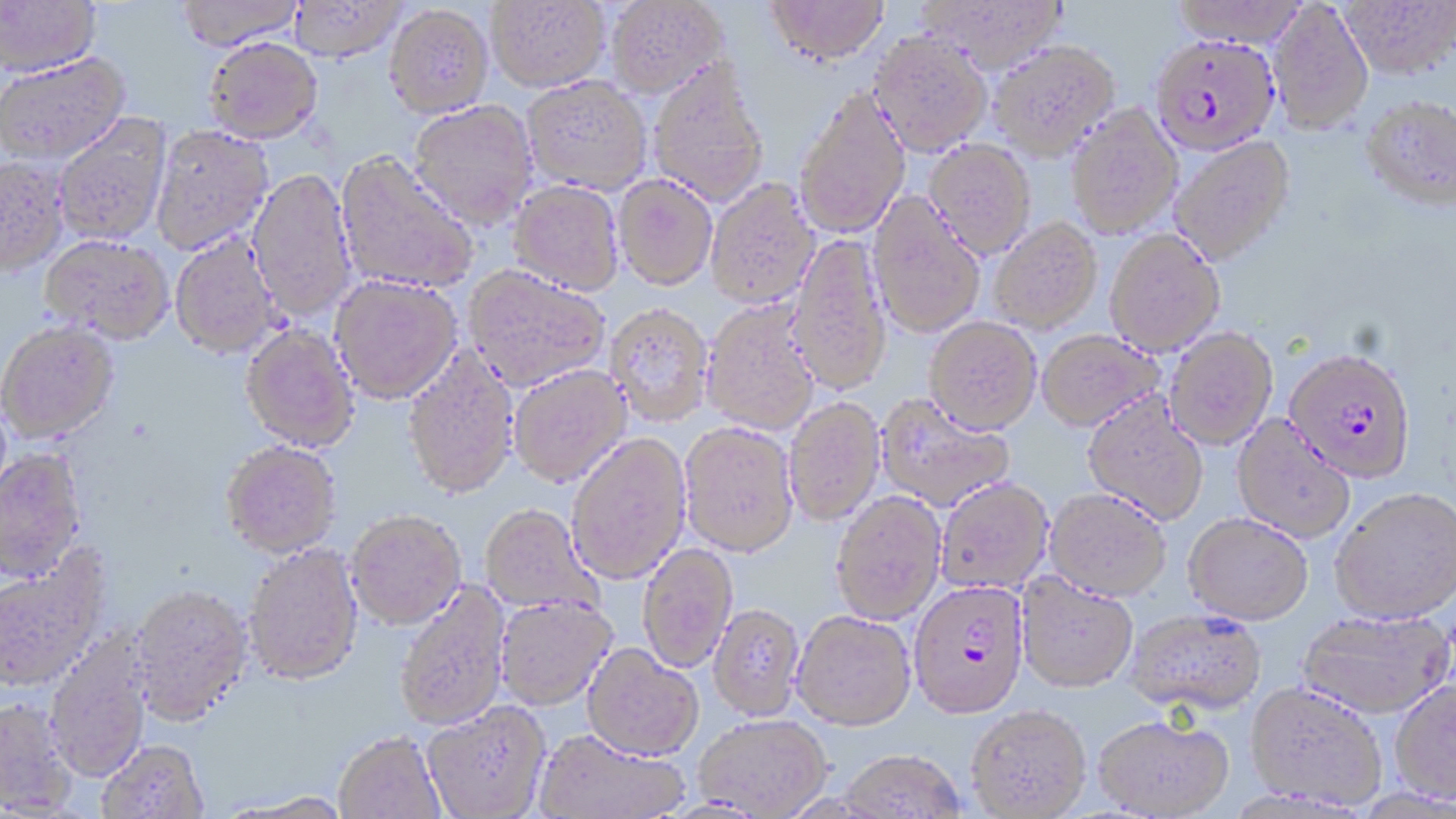 Approximate bounding boxes as named x1/y1/x2/y2 corners in pixels. Uninfected red blood cell locations: (x1=0, y1=0, x2=101, y2=77), (x1=176, y1=0, x2=304, y2=50), (x1=486, y1=0, x2=610, y2=92), (x1=606, y1=0, x2=728, y2=98), (x1=764, y1=0, x2=889, y2=66), (x1=918, y1=0, x2=1070, y2=73), (x1=1170, y1=0, x2=1308, y2=48), (x1=1339, y1=0, x2=1455, y2=78), (x1=288, y1=1, x2=407, y2=61), (x1=1268, y1=2, x2=1373, y2=134), (x1=384, y1=4, x2=494, y2=117), (x1=869, y1=31, x2=992, y2=156), (x1=204, y1=37, x2=323, y2=143), (x1=989, y1=39, x2=1120, y2=160), (x1=0, y1=52, x2=131, y2=164), (x1=648, y1=58, x2=770, y2=208), (x1=521, y1=75, x2=653, y2=194), (x1=794, y1=86, x2=911, y2=239), (x1=1360, y1=94, x2=1456, y2=211), (x1=408, y1=100, x2=539, y2=229), (x1=1066, y1=104, x2=1182, y2=238), (x1=53, y1=113, x2=172, y2=246), (x1=150, y1=124, x2=274, y2=256), (x1=1169, y1=136, x2=1296, y2=266), (x1=923, y1=139, x2=1037, y2=258), (x1=335, y1=151, x2=479, y2=294), (x1=0, y1=156, x2=69, y2=277), (x1=247, y1=167, x2=357, y2=322), (x1=613, y1=174, x2=718, y2=291), (x1=706, y1=178, x2=820, y2=308), (x1=508, y1=180, x2=624, y2=295), (x1=868, y1=192, x2=986, y2=338), (x1=990, y1=217, x2=1102, y2=333), (x1=1105, y1=229, x2=1224, y2=356), (x1=170, y1=233, x2=281, y2=358), (x1=41, y1=234, x2=174, y2=345), (x1=788, y1=234, x2=892, y2=396), (x1=464, y1=266, x2=610, y2=391), (x1=330, y1=275, x2=462, y2=403), (x1=702, y1=300, x2=820, y2=435), (x1=605, y1=304, x2=713, y2=425), (x1=924, y1=317, x2=1042, y2=434), (x1=0, y1=322, x2=120, y2=444), (x1=240, y1=324, x2=360, y2=452), (x1=1165, y1=327, x2=1279, y2=449), (x1=1036, y1=329, x2=1163, y2=431), (x1=402, y1=346, x2=520, y2=500), (x1=509, y1=365, x2=631, y2=487), (x1=876, y1=394, x2=1015, y2=512), (x1=1082, y1=394, x2=1208, y2=526), (x1=784, y1=397, x2=885, y2=526), (x1=1232, y1=416, x2=1355, y2=543), (x1=678, y1=422, x2=799, y2=556), (x1=566, y1=433, x2=691, y2=585), (x1=220, y1=440, x2=342, y2=558), (x1=0, y1=448, x2=87, y2=585), (x1=936, y1=478, x2=1054, y2=594), (x1=1044, y1=489, x2=1171, y2=601), (x1=1331, y1=489, x2=1456, y2=625), (x1=831, y1=491, x2=946, y2=624), (x1=479, y1=505, x2=603, y2=615), (x1=346, y1=509, x2=467, y2=630), (x1=1183, y1=513, x2=1313, y2=625), (x1=638, y1=542, x2=738, y2=673), (x1=243, y1=544, x2=364, y2=687), (x1=0, y1=549, x2=112, y2=695), (x1=1017, y1=573, x2=1139, y2=693), (x1=395, y1=581, x2=511, y2=732), (x1=129, y1=585, x2=253, y2=728), (x1=494, y1=596, x2=617, y2=711), (x1=708, y1=604, x2=805, y2=720), (x1=1124, y1=609, x2=1267, y2=717), (x1=1296, y1=609, x2=1453, y2=720), (x1=792, y1=611, x2=916, y2=733), (x1=45, y1=637, x2=152, y2=784), (x1=583, y1=644, x2=703, y2=761), (x1=1390, y1=682, x2=1456, y2=807), (x1=1245, y1=683, x2=1386, y2=811), (x1=1, y1=701, x2=76, y2=817), (x1=423, y1=703, x2=551, y2=819), (x1=966, y1=707, x2=1092, y2=818), (x1=694, y1=715, x2=831, y2=817), (x1=1093, y1=716, x2=1234, y2=818), (x1=534, y1=731, x2=688, y2=819), (x1=334, y1=734, x2=446, y2=819), (x1=98, y1=744, x2=209, y2=819), (x1=838, y1=751, x2=967, y2=818), (x1=228, y1=794, x2=355, y2=819). Plasmodium falciparum-infected red blood cell locations: (x1=1151, y1=33, x2=1280, y2=154), (x1=1284, y1=348, x2=1417, y2=482), (x1=908, y1=580, x2=1030, y2=720). Slide-level diagnosis: Plasmodium falciparum. Image is 1456×819 pixels. 1000x magnification. One field of a larger specimen. May-Grünwald-Giemsa stain. Thin blood smear. Optical microscopy.